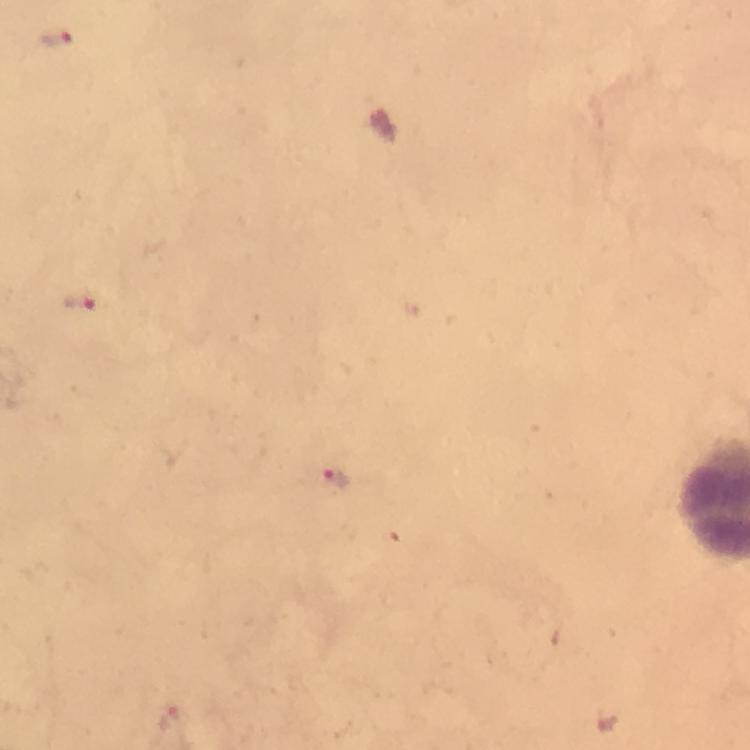
Approximate centers as (x, y) in pixels. Plasmodium parasite locations: (56, 40), (83, 306), (330, 478). A crop from one field of view. Image is 750×750 pixels. From a diagnostic examination for malaria. 100x magnification. Photographed with a smartphone mounted on the microscope. Immersion oil was used. Thick blood smear. Giemsa stain.